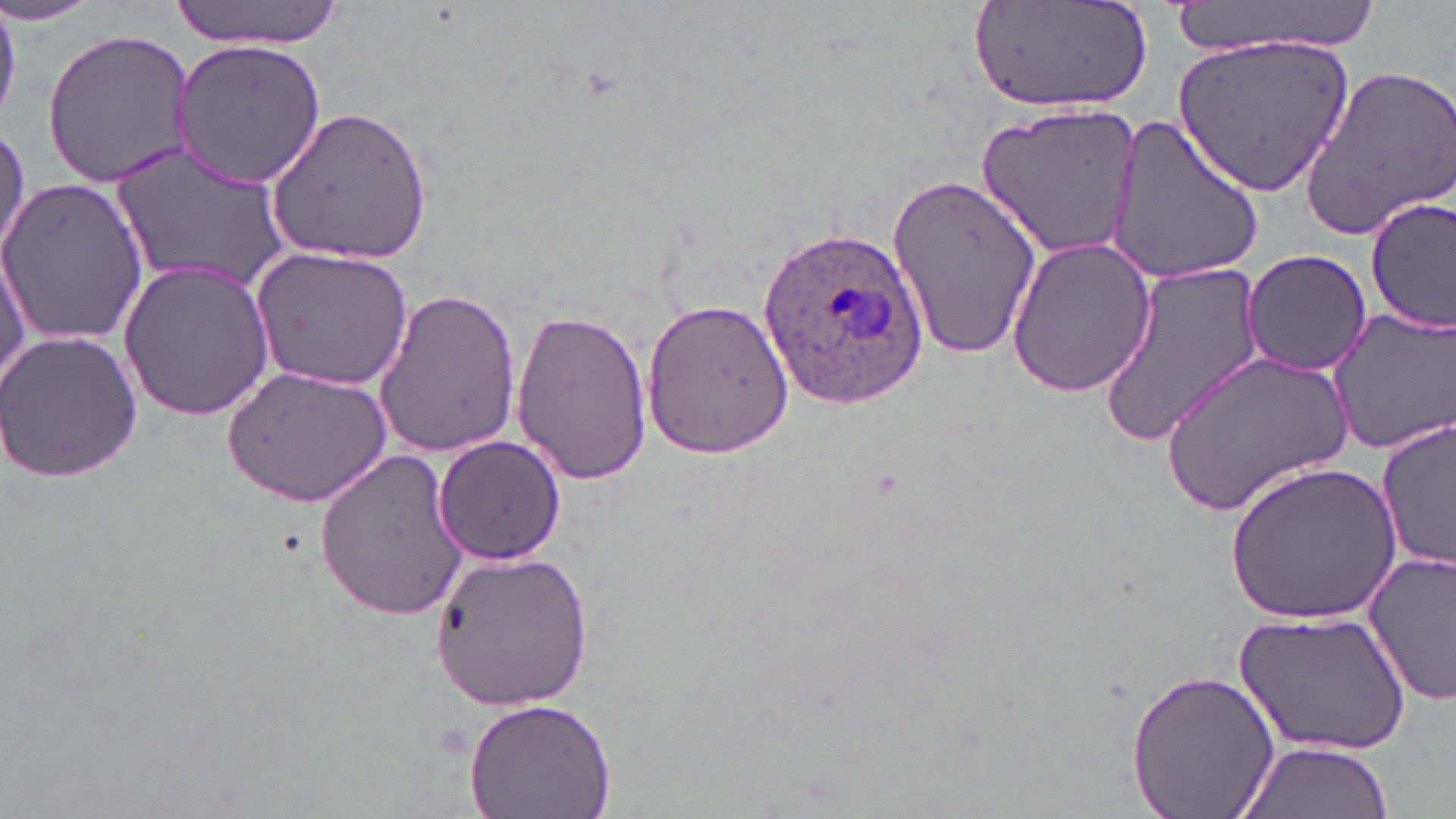
Approximate bounding boxes as (x1,y1)-(x2,y2) corner pairs in pixels. Uninfected red blood cell locations: (171,0)-(349,50), (1164,0)-(1385,60), (972,3)-(1153,114), (41,29)-(197,188), (1173,29)-(1357,196), (171,36)-(328,190), (1301,62)-(1456,239), (975,102)-(1144,258), (268,104)-(434,265), (1101,111)-(1265,286), (0,120)-(30,272), (112,146)-(289,294), (885,172)-(1041,361), (0,177)-(153,345), (1364,194)-(1455,338), (2,236)-(34,397), (1007,237)-(1159,396), (253,246)-(415,389), (1242,248)-(1372,377), (116,256)-(275,422), (1096,259)-(1266,449), (370,286)-(522,457), (641,298)-(794,459), (1326,305)-(1456,456), (510,306)-(653,487), (1,330)-(142,482), (1159,347)-(1353,520), (225,364)-(393,508), (1378,420)-(1454,570), (432,434)-(565,566), (313,449)-(474,622), (1226,458)-(1403,626), (1361,545)-(1456,707), (431,549)-(595,711), (1235,610)-(1410,757), (1125,667)-(1282,819), (461,697)-(619,819), (1234,739)-(1393,819). Plasmodium ovale-infected red blood cell locations: (760,226)-(930,402). Slide-level diagnosis: Plasmodium ovale. Optical microscopy. Thin blood smear. May-Grünwald-Giemsa-stained preparation. Image is 1456×819 pixels. One field of a larger specimen. 1000x magnification.